Name the parasite shown.
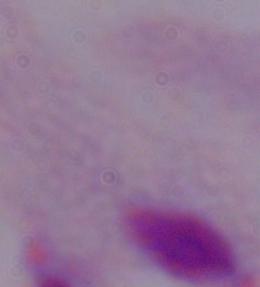

This is a trichomonad.

magnification: 1000x
modality: micrograph